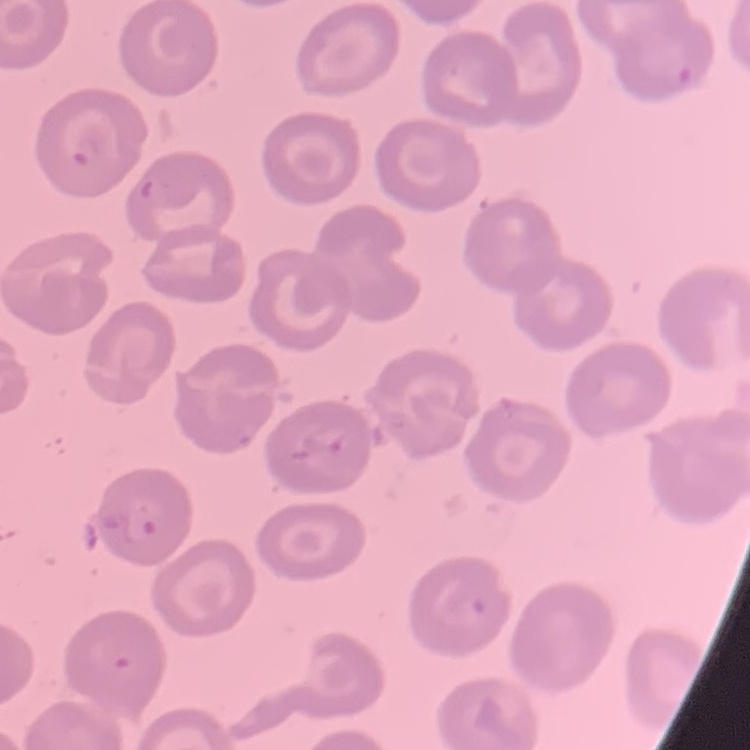
The red blood cells exhibit no rouleaux formation. Stained with either Field's or Giemsa. Square crop of a larger photomicrograph. Thin blood smear.